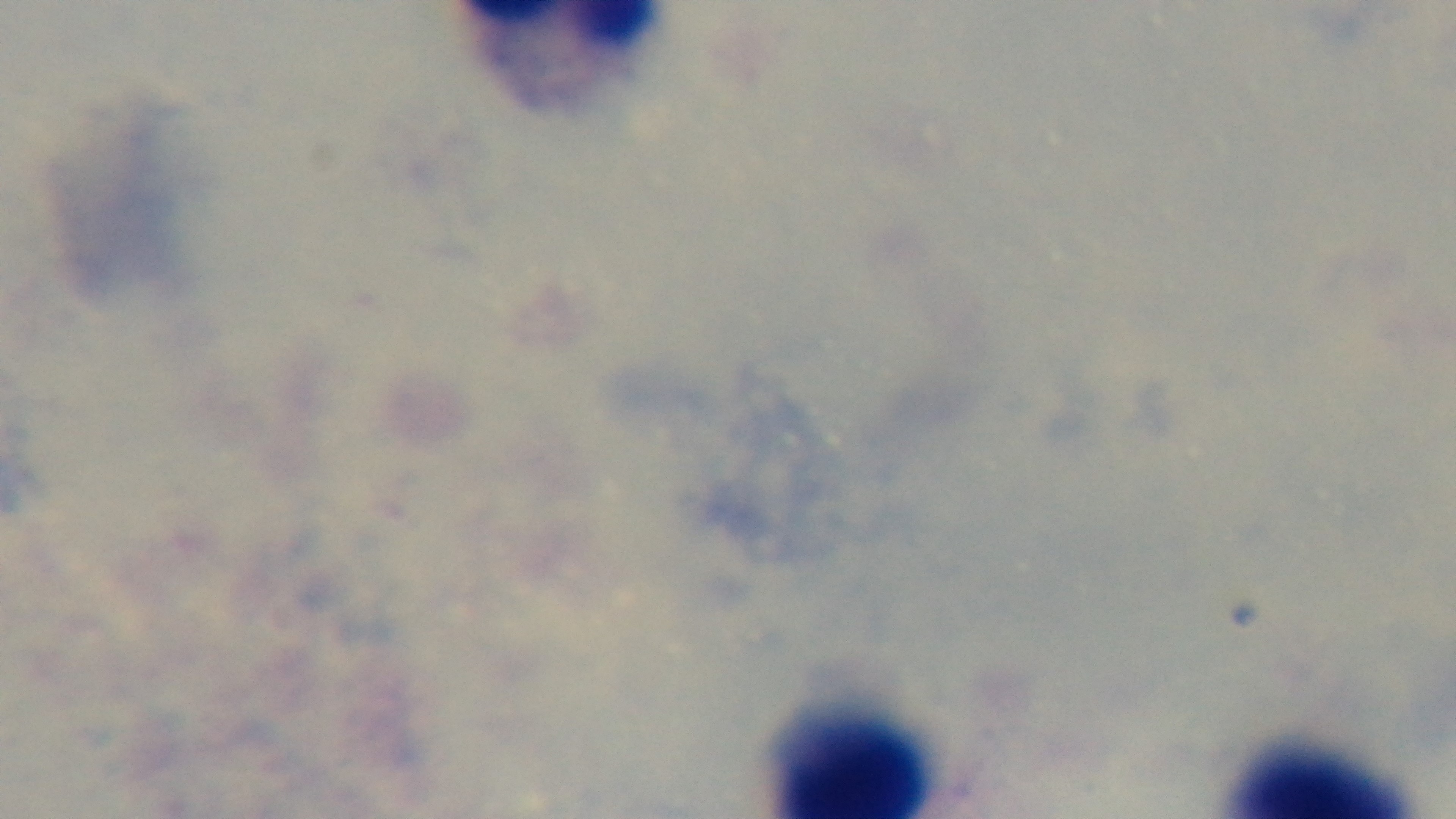
Mounted 4K digital camera. Photomicrograph. Single field of view. Oil-immersion objective, 100x. Malaria status: uninfected. Giemsa-stained. Preparation: thick blood film.